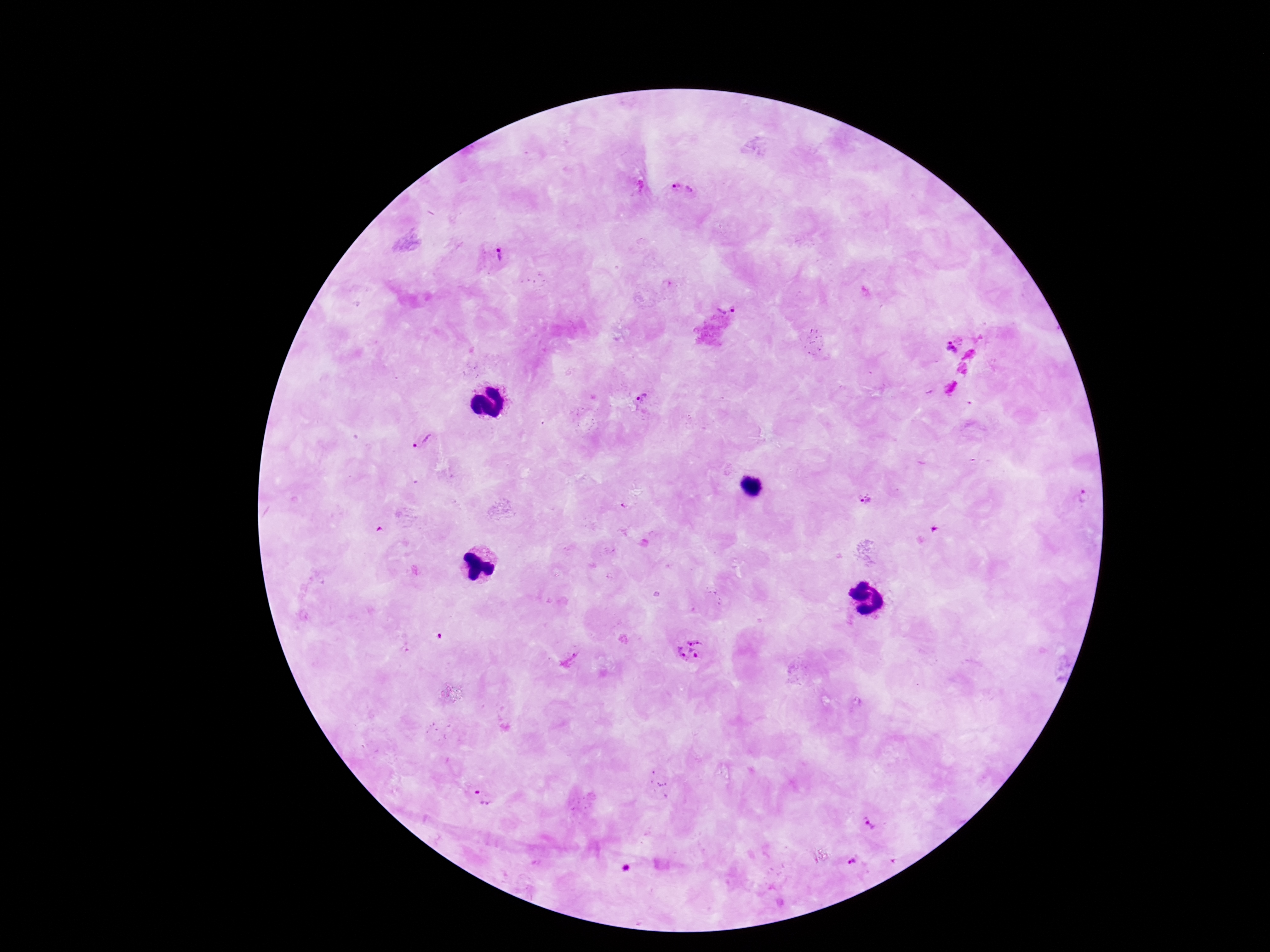

Approximate centers as [x, y] in pixels.
Summary:
  - Plasmodium parasite locations: [682, 190], [494, 254], [726, 303], [952, 346], [641, 399], [421, 440], [1082, 497], [866, 498], [689, 649], [483, 799], [872, 820], [854, 860]
  - Preparation: thick blood film
  - Magnification: 100x
  - Stain: Giemsa
  - Field of view: one from this slide
  - Image size: 1270×952 pixels
  - Capture: smartphone camera through the microscope eyepiece
  - Patient malaria status: positive